Give the preparation type.
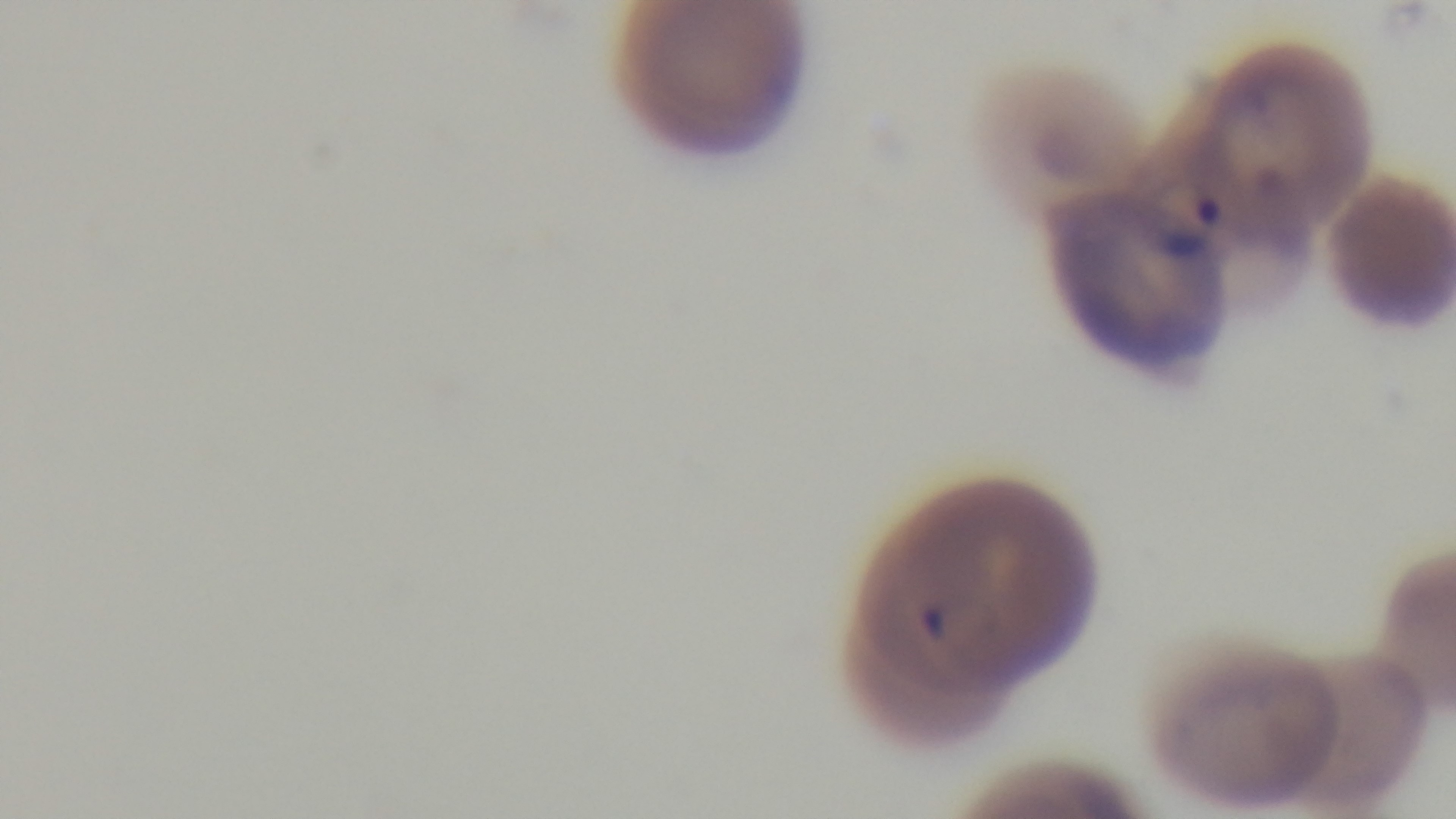

Thin.

modality = light microscopy
stain = Giemsa
capture = mounted 4K digital camera
malaria status = infected
objective = 100x oil immersion
field of view = one from the slide